Assess this cell for malaria.
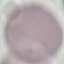

It is uninfected.

Summary:
  - Preparation: thin blood film
  - Stain: Giemsa
  - Image type: automatically extracted cell patch, resized to 64 × 64 pixels
  - Capture: smartphone camera at the microscope eyepiece